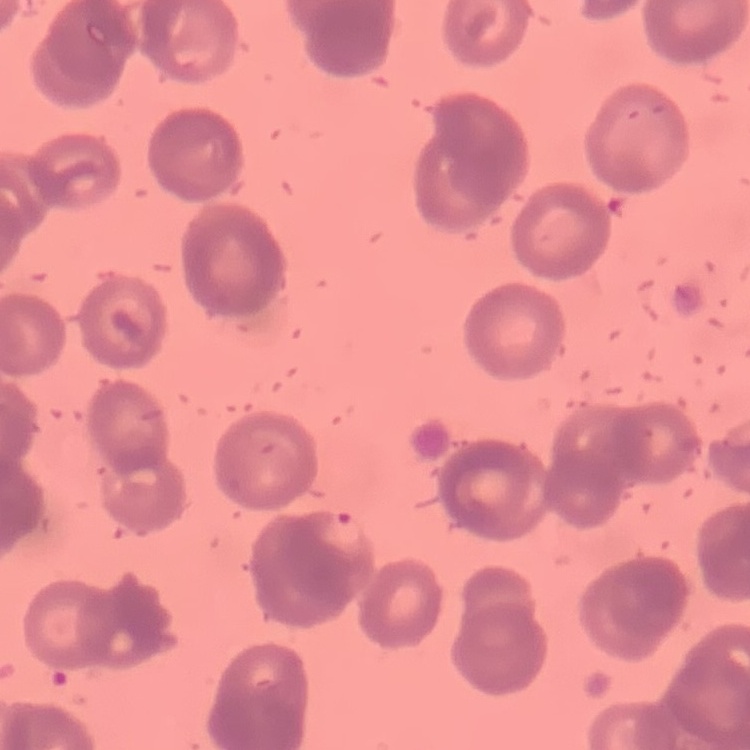

Summary:
  - Red blood cell morphology: rouleaux formation
  - Preparation: thin blood film
  - Image type: square crop of a larger photomicrograph
  - Stain: Field's or Giemsa